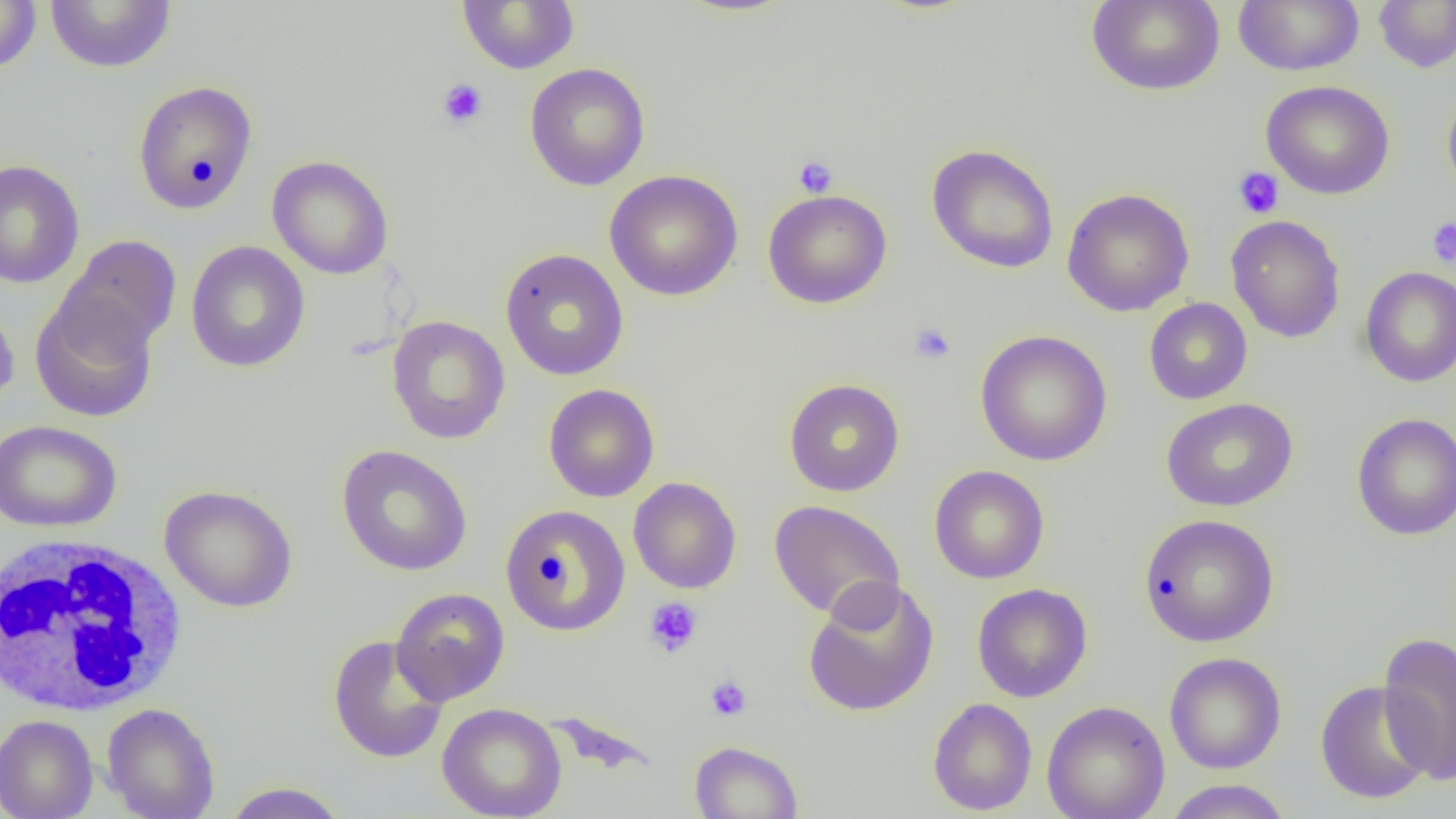 Approximate bounding boxes as named x1/y1/x2/y2 corners in pixels. White blood cell locations: (x1=1, y1=534, x2=189, y2=717). Platelet locations: (x1=437, y1=78, x2=488, y2=129), (x1=793, y1=155, x2=838, y2=197), (x1=1233, y1=167, x2=1284, y2=219), (x1=1426, y1=217, x2=1456, y2=269), (x1=908, y1=322, x2=956, y2=365), (x1=644, y1=596, x2=704, y2=658), (x1=705, y1=675, x2=752, y2=721). Uninfected red blood cell locations: (x1=45, y1=0, x2=176, y2=73), (x1=458, y1=0, x2=579, y2=75), (x1=1086, y1=0, x2=1225, y2=96), (x1=1233, y1=0, x2=1365, y2=76), (x1=1373, y1=0, x2=1456, y2=73), (x1=0, y1=1, x2=42, y2=74), (x1=524, y1=63, x2=651, y2=191), (x1=132, y1=80, x2=258, y2=214), (x1=1260, y1=80, x2=1395, y2=200), (x1=1442, y1=87, x2=1456, y2=200), (x1=926, y1=143, x2=1059, y2=274), (x1=266, y1=155, x2=394, y2=280), (x1=0, y1=159, x2=85, y2=289), (x1=604, y1=170, x2=743, y2=301), (x1=1062, y1=188, x2=1195, y2=316), (x1=763, y1=189, x2=892, y2=309), (x1=1226, y1=215, x2=1346, y2=343), (x1=56, y1=235, x2=182, y2=356), (x1=185, y1=240, x2=310, y2=373), (x1=499, y1=248, x2=630, y2=382), (x1=1359, y1=266, x2=1456, y2=387), (x1=30, y1=293, x2=159, y2=423), (x1=0, y1=298, x2=19, y2=413), (x1=1143, y1=298, x2=1253, y2=404), (x1=386, y1=315, x2=510, y2=444), (x1=974, y1=330, x2=1113, y2=466), (x1=783, y1=378, x2=905, y2=497), (x1=543, y1=384, x2=660, y2=503), (x1=1160, y1=397, x2=1298, y2=512), (x1=1351, y1=413, x2=1456, y2=540), (x1=0, y1=419, x2=122, y2=532), (x1=336, y1=445, x2=473, y2=576), (x1=929, y1=465, x2=1049, y2=584), (x1=628, y1=477, x2=741, y2=594), (x1=159, y1=484, x2=298, y2=613), (x1=768, y1=500, x2=906, y2=623), (x1=500, y1=504, x2=631, y2=635), (x1=1138, y1=514, x2=1279, y2=647), (x1=802, y1=579, x2=940, y2=717), (x1=972, y1=583, x2=1093, y2=703), (x1=390, y1=587, x2=510, y2=705), (x1=1378, y1=632, x2=1456, y2=785), (x1=327, y1=634, x2=450, y2=765), (x1=1164, y1=652, x2=1286, y2=774), (x1=1315, y1=680, x2=1434, y2=804), (x1=927, y1=697, x2=1037, y2=815), (x1=1042, y1=701, x2=1170, y2=819), (x1=102, y1=702, x2=220, y2=819), (x1=437, y1=702, x2=567, y2=819), (x1=0, y1=715, x2=98, y2=819), (x1=688, y1=740, x2=803, y2=819), (x1=1162, y1=779, x2=1294, y2=819), (x1=221, y1=782, x2=350, y2=819). Slide-level diagnosis: no evidence of blood parasites. Thin blood smear. 1000x magnification. One field of a larger specimen. Image is 1456×819 pixels. Light microscopy.